State which malaria species this is.
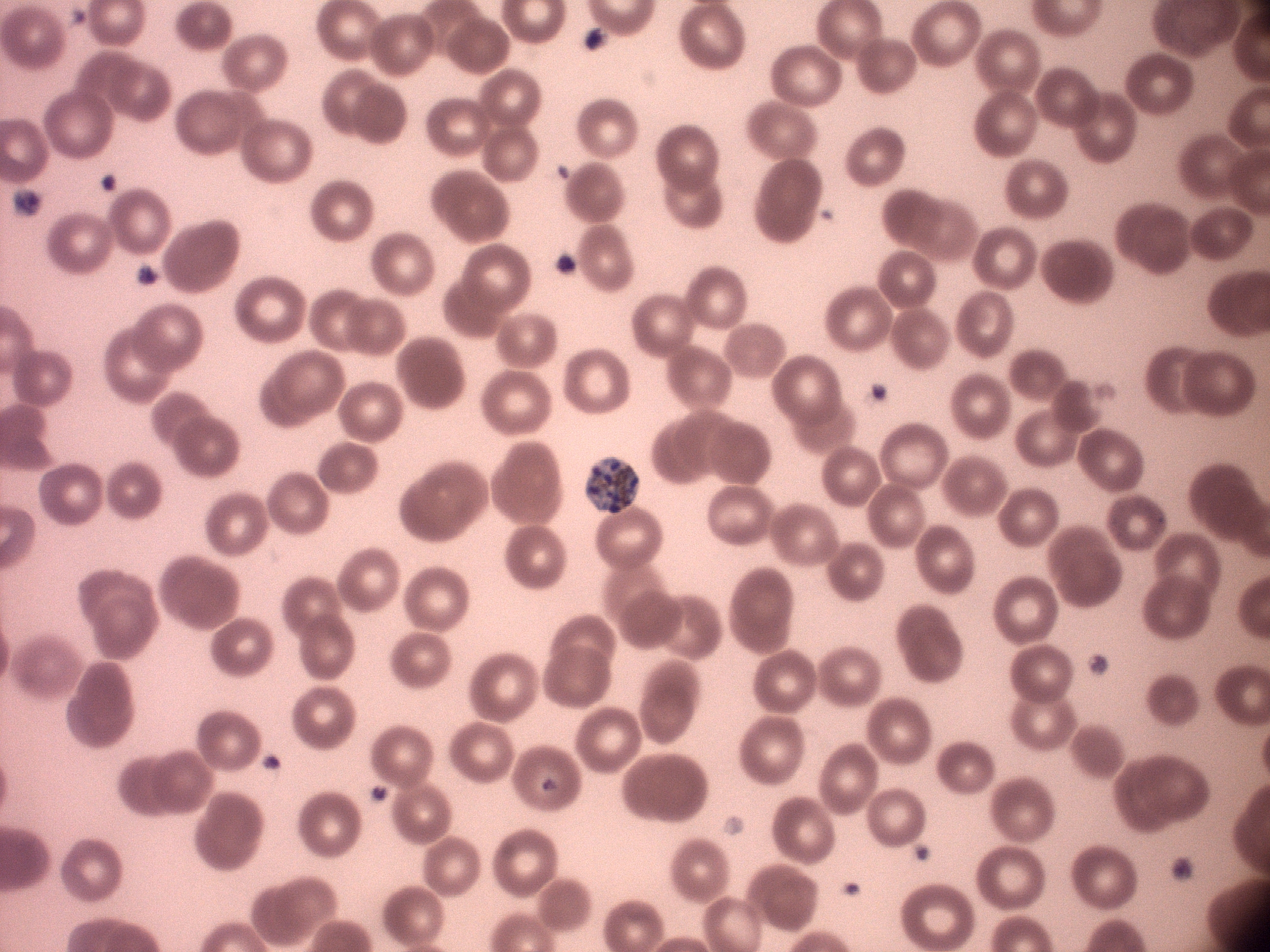

Plasmodium malariae.

magnification = 100x
microscope = Leica DM2000 with built-in camera
schizont locations = approximate bounding boxes as (x1,y1)-(x2,y2) corner pairs in pixels, from the source annotation, which is not necessarily exhaustive: (585,457)-(639,513)
preparation = thin blood film
image size = 1270×952 pixels
stain = Giemsa
field of view = single